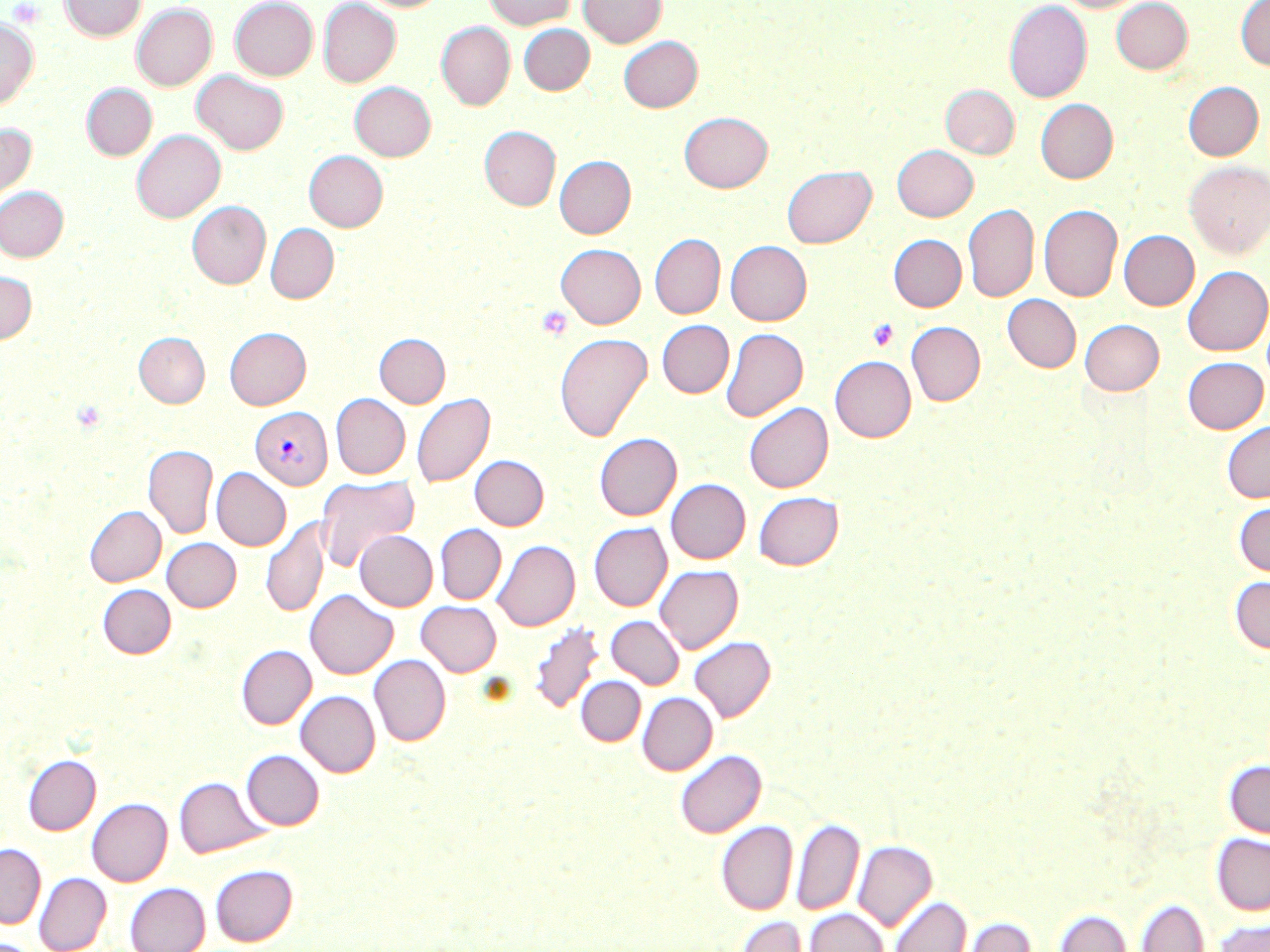
Approximate bounding boxes as [x1, y1, x2, y2] in pixels. Platelet locations: [8, 1, 43, 27], [537, 306, 573, 341], [867, 318, 899, 352]. Plasmodium vivax-infected red blood cell locations: [250, 406, 332, 489]. Uninfected red blood cell locations: [60, 0, 145, 40], [230, 0, 318, 81], [318, 0, 401, 87], [358, 0, 447, 12], [484, 0, 575, 29], [579, 0, 666, 47], [1058, 0, 1145, 13], [1110, 0, 1193, 74], [1004, 1, 1092, 103], [1235, 1, 1270, 70], [132, 4, 317, 87], [132, 5, 217, 91], [0, 18, 38, 111], [437, 22, 515, 110], [519, 24, 594, 94], [618, 36, 702, 112], [192, 70, 288, 154], [1183, 81, 1263, 160], [350, 82, 435, 162], [82, 84, 156, 160], [941, 85, 1019, 159], [1036, 99, 1118, 183], [679, 111, 772, 192], [0, 122, 36, 208], [480, 126, 560, 210], [131, 130, 225, 223], [893, 145, 978, 221], [304, 151, 387, 231], [554, 156, 635, 238], [1184, 161, 1270, 258], [782, 164, 876, 248], [0, 187, 68, 262], [187, 200, 270, 289], [963, 204, 1038, 302], [1039, 204, 1123, 302], [265, 223, 338, 303], [1119, 230, 1199, 310], [650, 233, 725, 319], [889, 234, 966, 311], [726, 240, 811, 325], [556, 243, 645, 328], [1183, 265, 1270, 355], [0, 272, 37, 344], [1003, 294, 1081, 372], [1080, 319, 1163, 395], [657, 320, 734, 398], [906, 321, 985, 405], [225, 327, 311, 409], [721, 327, 807, 421], [134, 332, 210, 407], [375, 333, 450, 407], [555, 333, 652, 441], [830, 356, 916, 442], [1182, 356, 1268, 433], [412, 392, 495, 487], [331, 394, 410, 479], [744, 402, 832, 492], [1221, 420, 1270, 502], [594, 433, 681, 520], [143, 444, 218, 538], [470, 455, 549, 530], [212, 468, 291, 550], [316, 474, 419, 571], [666, 478, 750, 563], [753, 491, 843, 570], [1233, 500, 1270, 577], [84, 505, 166, 586], [260, 516, 329, 618], [589, 522, 672, 610], [435, 524, 506, 604], [355, 530, 437, 611], [162, 538, 241, 611], [492, 540, 580, 630], [654, 564, 743, 653], [1229, 576, 1270, 654], [98, 584, 175, 658], [305, 589, 398, 678], [417, 601, 501, 676], [606, 615, 684, 689], [530, 621, 604, 715], [689, 636, 775, 721], [237, 645, 316, 729], [369, 654, 451, 745], [576, 676, 645, 746], [296, 691, 380, 777], [637, 692, 717, 775], [675, 749, 765, 837], [242, 750, 323, 829], [23, 754, 100, 835], [1224, 759, 1270, 839], [175, 776, 269, 857], [87, 798, 172, 886], [791, 817, 864, 915], [716, 820, 797, 914], [1212, 833, 1270, 915], [852, 840, 937, 931], [0, 843, 45, 928], [210, 864, 297, 946], [35, 872, 111, 952], [125, 882, 210, 952], [890, 896, 971, 952], [1134, 899, 1209, 952], [804, 908, 888, 952], [1053, 908, 1131, 952], [733, 915, 811, 952], [959, 916, 1036, 952], [1211, 917, 1270, 952], [0, 939, 39, 952]. Slide-level diagnosis: Plasmodium vivax. May-Grünwald-Giemsa stain. Single field of view. 1000x magnification. Thin blood film. Optical microscopy. Image is 1270×952 pixels.